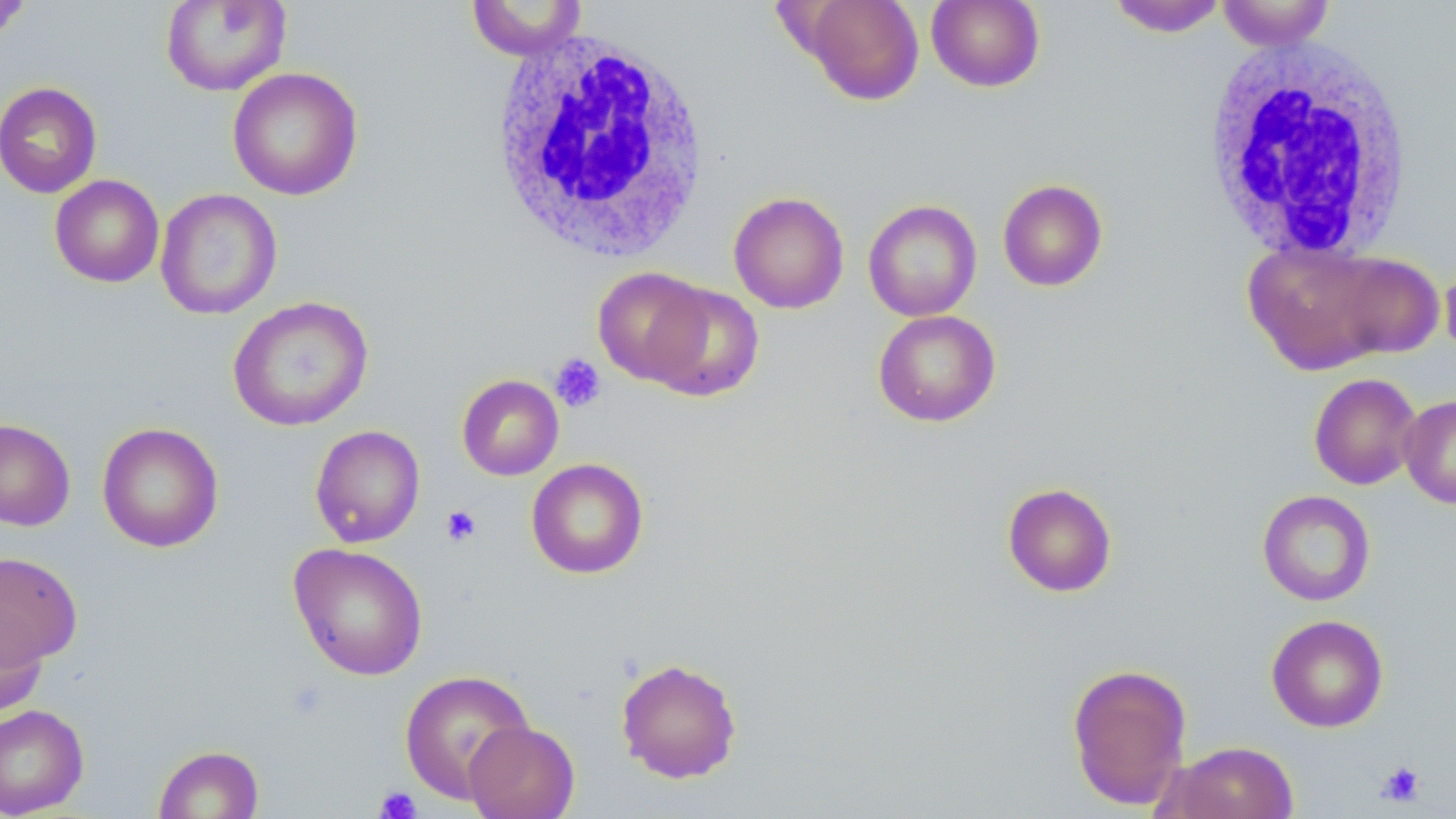
Approximate bounding boxes as [x1, y1, x2, y2] in pixels. Platelet locations: [550, 353, 607, 412], [441, 504, 483, 547], [1375, 760, 1427, 807], [374, 786, 422, 818]. White blood cell locations: [487, 29, 711, 264], [1198, 35, 1416, 263]. Uninfected red blood cell locations: [799, 0, 925, 105], [1106, 0, 1230, 37], [0, 1, 33, 41], [161, 1, 291, 96], [465, 1, 588, 60], [926, 1, 1046, 92], [1217, 1, 1335, 51], [227, 67, 363, 201], [0, 81, 102, 198], [49, 174, 164, 288], [997, 178, 1108, 291], [155, 188, 282, 319], [729, 192, 849, 314], [864, 199, 982, 321], [1243, 239, 1397, 375], [1328, 252, 1444, 360], [1440, 260, 1456, 357], [592, 267, 715, 386], [642, 280, 764, 402], [228, 296, 373, 431], [873, 309, 1001, 427], [1309, 373, 1422, 490], [456, 374, 564, 480], [1399, 394, 1456, 508], [0, 419, 75, 531], [96, 422, 223, 552], [310, 425, 425, 547], [526, 458, 649, 579], [1002, 482, 1117, 597], [1257, 490, 1376, 606], [288, 542, 429, 682], [0, 552, 83, 669], [0, 608, 48, 717], [1266, 614, 1389, 733], [615, 657, 743, 783], [1066, 662, 1193, 810], [399, 669, 535, 803], [0, 704, 89, 817], [464, 721, 580, 819], [1158, 741, 1300, 819], [153, 744, 264, 819]. Slide-level diagnosis: no evidence of blood parasites. 1000x magnification. Thin blood film. Image is 1456×819 pixels. May-Grünwald-Giemsa stain. One field of a larger specimen. Light microscopy.